Give the position of every Plasmodium parasite visible.
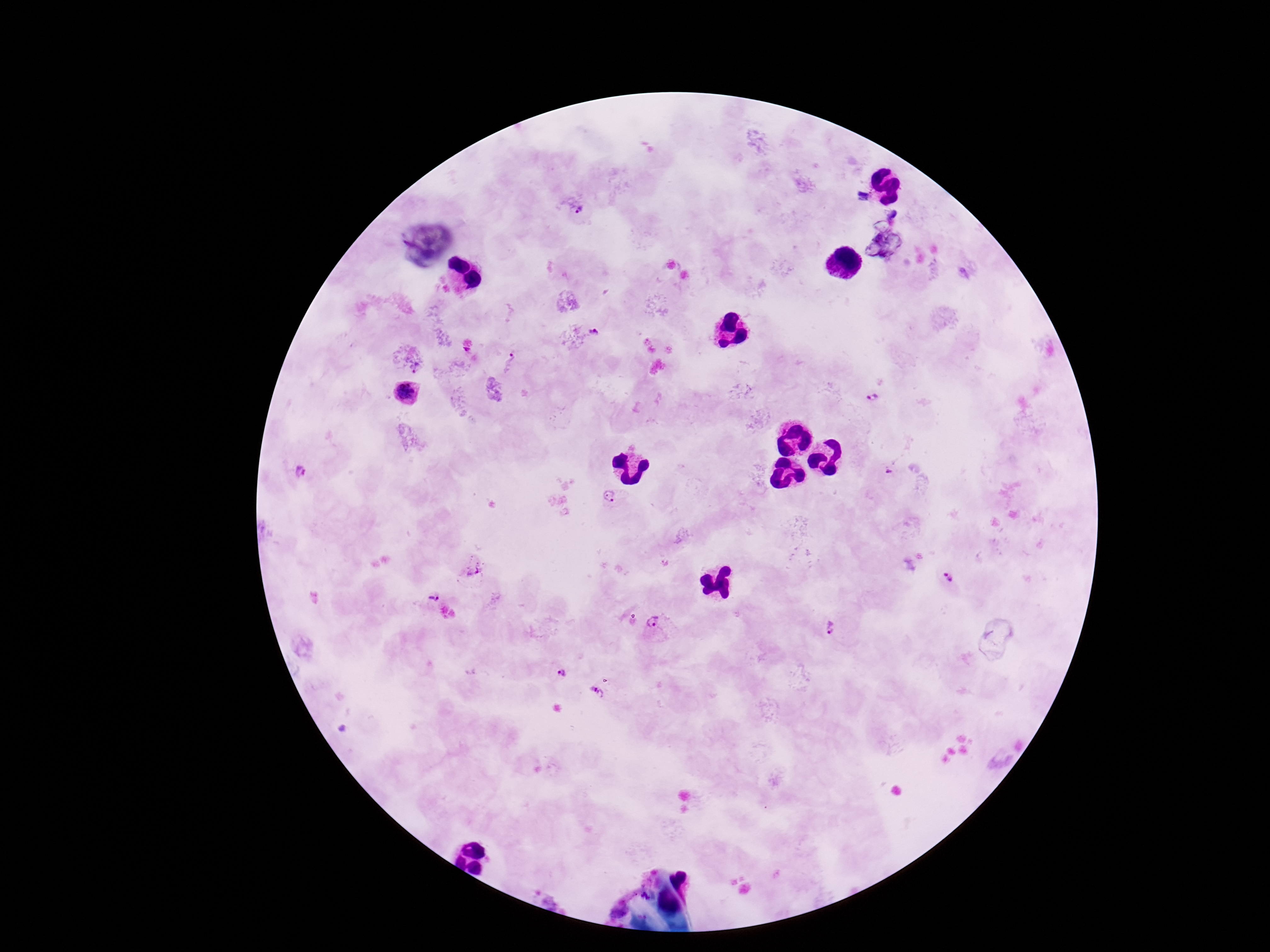

Approximate centers as (x, y) in pixels.
Plasmodium parasites: (577, 210), (595, 334), (510, 362), (406, 392), (881, 401), (302, 472), (610, 496), (473, 568), (948, 576), (429, 598), (656, 621), (830, 627), (562, 673), (594, 693).

Single field of view. Patient malaria status: positive. Photographed through the microscope eyepiece with a smartphone camera. Thick blood film. Giemsa stain. 100x magnification. Image is 1270×952 pixels.